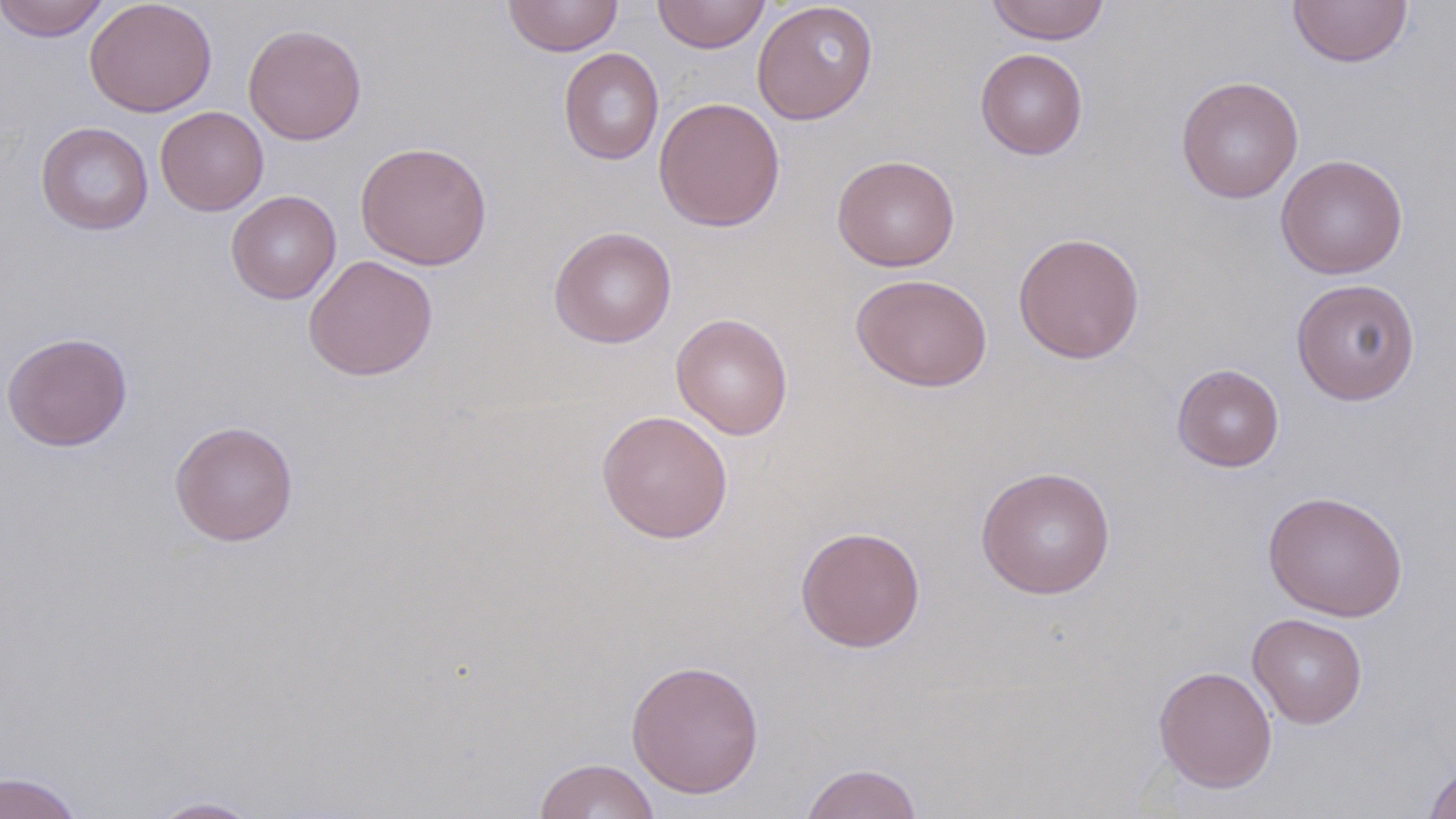
slide-level diagnosis = no evidence of blood parasites
stain = May-Grünwald-Giemsa
modality = optical microscopy
uninfected red blood cell locations = approximate bounding boxes as [x1, y1, x2, y2] in pixels: [0, 0, 110, 42], [84, 0, 217, 117], [503, 0, 623, 56], [652, 0, 771, 54], [985, 0, 1111, 45], [1287, 0, 1413, 67], [752, 1, 879, 125], [242, 24, 367, 145], [559, 47, 664, 166], [975, 48, 1088, 160], [1176, 76, 1303, 204], [653, 97, 786, 232], [155, 106, 269, 216], [35, 121, 154, 236], [355, 141, 493, 270], [832, 154, 960, 272], [1275, 154, 1408, 279], [226, 190, 341, 304], [549, 226, 677, 349], [1012, 232, 1145, 364], [303, 254, 438, 381], [850, 273, 993, 392], [1290, 278, 1421, 405], [671, 313, 793, 440], [1, 331, 133, 452], [1172, 364, 1284, 472], [596, 409, 733, 543], [169, 419, 298, 546], [976, 466, 1115, 599], [1262, 490, 1408, 622], [794, 525, 926, 653], [1247, 612, 1367, 728], [625, 658, 765, 800], [1153, 664, 1278, 794], [534, 758, 661, 819], [799, 762, 924, 819], [1423, 762, 1456, 819], [0, 772, 83, 818], [146, 796, 265, 818]
field of view = single
magnification = 1000x
preparation = thin blood smear
image size = 1456×819 pixels